State which parasite is depicted.
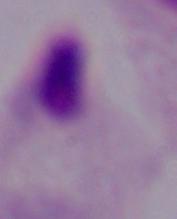

A trichomonad.

Micrograph. Captured at 1000x magnification.